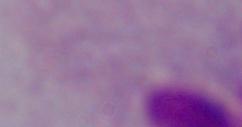 Micrograph. 1000x magnification. A trichomonad is shown.